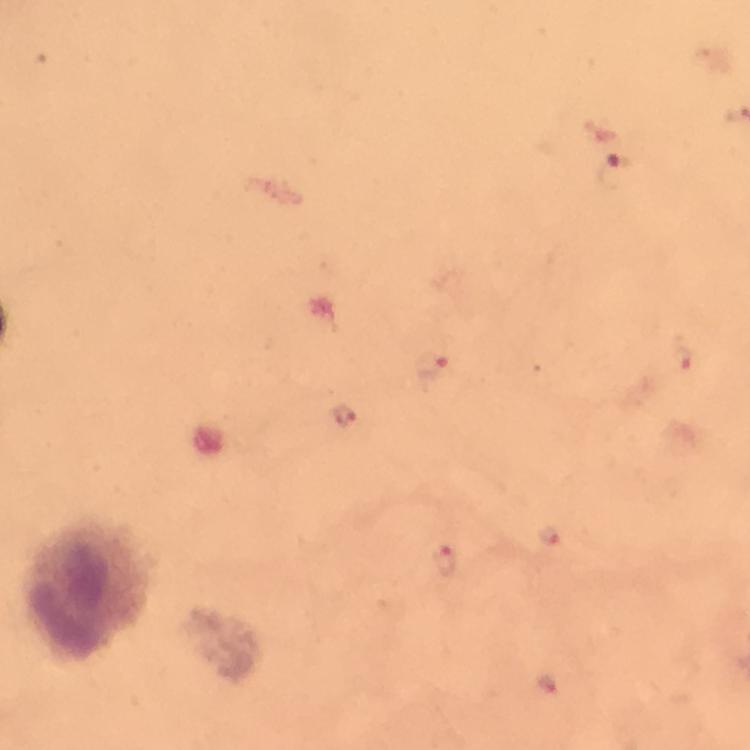
Approximate centers as [x, y] in pixels. Malaria parasite locations: [615, 170], [683, 359], [436, 365], [549, 536], [446, 561]. Leukocyte locations: [85, 591]. Image is 750×750 pixels. Photographed with a smartphone mounted on the microscope. Giemsa stain. From a diagnostic examination for malaria. Immersion oil applied. At 100x magnification. Thick blood film. A crop from one field of view.